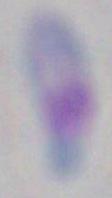
identification: Toxoplasma gondii
modality: photomicrograph
magnification: 1000x